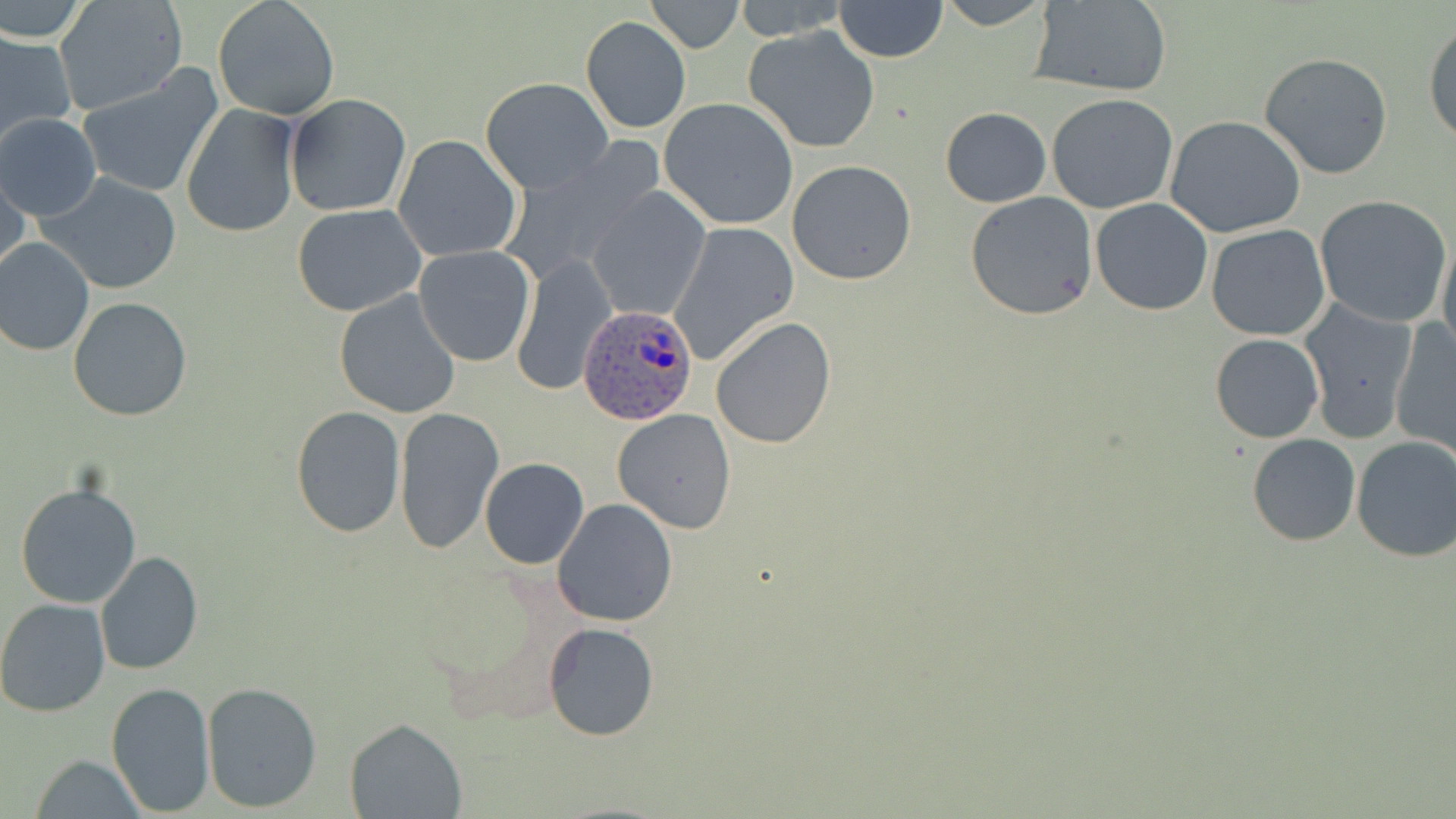
Summary:
  - Coordinate format: approximate bounding boxes as named x1/y1/x2/y2 corners in pixels
  - Plasmodium ovale-infected red blood cell locations: (x1=580, y1=303, x2=698, y2=426)
  - Uninfected red blood cell locations: (x1=0, y1=0, x2=92, y2=45), (x1=53, y1=0, x2=189, y2=117), (x1=212, y1=0, x2=341, y2=121), (x1=645, y1=0, x2=743, y2=53), (x1=732, y1=0, x2=849, y2=38), (x1=834, y1=0, x2=947, y2=62), (x1=934, y1=0, x2=1056, y2=30), (x1=1028, y1=1, x2=1173, y2=96), (x1=581, y1=16, x2=691, y2=133), (x1=1424, y1=19, x2=1456, y2=147), (x1=741, y1=25, x2=882, y2=153), (x1=0, y1=30, x2=76, y2=147), (x1=1259, y1=53, x2=1393, y2=178), (x1=78, y1=68, x2=223, y2=198), (x1=481, y1=77, x2=614, y2=194), (x1=285, y1=93, x2=411, y2=217), (x1=1046, y1=93, x2=1179, y2=213), (x1=659, y1=98, x2=799, y2=231), (x1=181, y1=104, x2=301, y2=237), (x1=941, y1=107, x2=1051, y2=206), (x1=0, y1=112, x2=102, y2=222), (x1=1165, y1=116, x2=1308, y2=240), (x1=393, y1=134, x2=523, y2=263), (x1=499, y1=141, x2=663, y2=285), (x1=788, y1=160, x2=917, y2=283), (x1=1, y1=168, x2=30, y2=283), (x1=37, y1=172, x2=183, y2=296), (x1=585, y1=186, x2=710, y2=322), (x1=965, y1=192, x2=1100, y2=321), (x1=1315, y1=194, x2=1451, y2=327), (x1=1090, y1=199, x2=1213, y2=316), (x1=292, y1=204, x2=426, y2=316), (x1=667, y1=222, x2=799, y2=365), (x1=1206, y1=224, x2=1331, y2=342), (x1=1439, y1=236, x2=1456, y2=364), (x1=0, y1=237, x2=94, y2=357), (x1=414, y1=246, x2=536, y2=367), (x1=512, y1=254, x2=613, y2=396), (x1=333, y1=290, x2=461, y2=420), (x1=68, y1=297, x2=194, y2=422), (x1=1298, y1=300, x2=1418, y2=446), (x1=710, y1=317, x2=837, y2=450), (x1=1389, y1=318, x2=1455, y2=458), (x1=1210, y1=334, x2=1325, y2=443), (x1=290, y1=406, x2=407, y2=538), (x1=394, y1=406, x2=505, y2=554), (x1=613, y1=410, x2=738, y2=533), (x1=1247, y1=434, x2=1361, y2=546), (x1=1351, y1=436, x2=1456, y2=562), (x1=479, y1=458, x2=588, y2=570), (x1=15, y1=482, x2=142, y2=608), (x1=551, y1=497, x2=677, y2=627), (x1=95, y1=550, x2=204, y2=675), (x1=0, y1=599, x2=113, y2=718), (x1=544, y1=622, x2=660, y2=743), (x1=105, y1=681, x2=216, y2=816), (x1=201, y1=682, x2=322, y2=812), (x1=345, y1=717, x2=467, y2=817), (x1=32, y1=754, x2=145, y2=819)
  - Slide-level diagnosis: Plasmodium ovale
  - Field of view: single
  - Stain: May-Grünwald-Giemsa
  - Magnification: 1000x
  - Modality: light microscopy
  - Image size: 1456×819 pixels
  - Preparation: thin blood smear